Locate every Plasmodium parasite and identify its life-cycle stage.
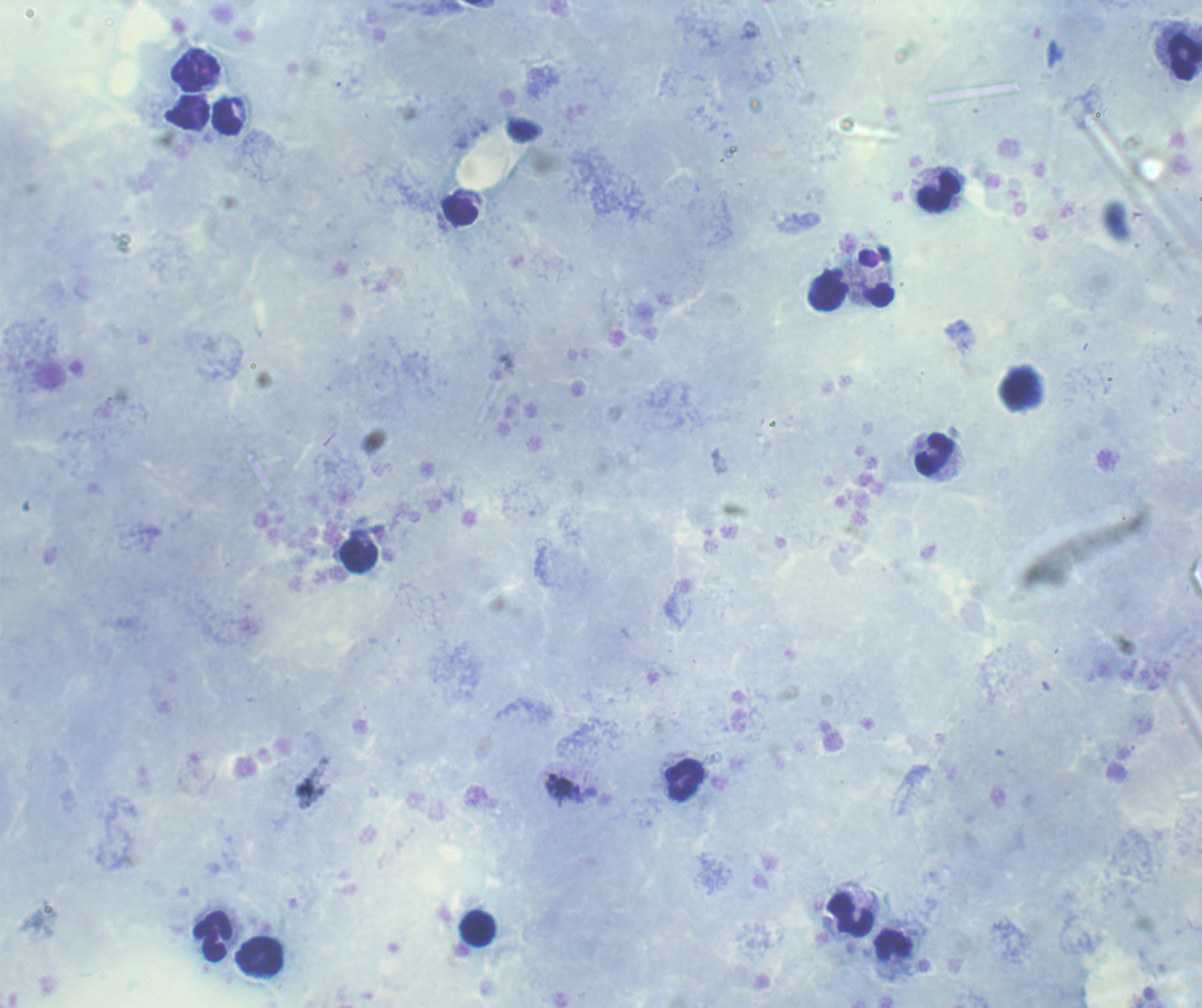
Approximate object centers, in pixels from the top-left corner.
Trophozoites: (x=551, y=784), (x=571, y=791).
No schizont or gametocyte forms observed.

Approximate object centers, in pixels from the top-left corner.
Summary:
  - Leukocyte locations: (x=1185, y=57), (x=196, y=71), (x=187, y=111), (x=227, y=116), (x=939, y=192), (x=459, y=210), (x=875, y=278), (x=827, y=293), (x=935, y=453), (x=358, y=555), (x=684, y=779), (x=849, y=914), (x=478, y=928), (x=213, y=937), (x=894, y=944), (x=260, y=956)
  - Context: previously used in a real diagnosis
  - Magnification: 100x
  - Field of view: one from this slide
  - Stain: Romanowsky
  - Image size: 1202×1008 pixels
  - Coloration quality: good
  - Preparation: thick blood smear
  - Background quality: satisfactory